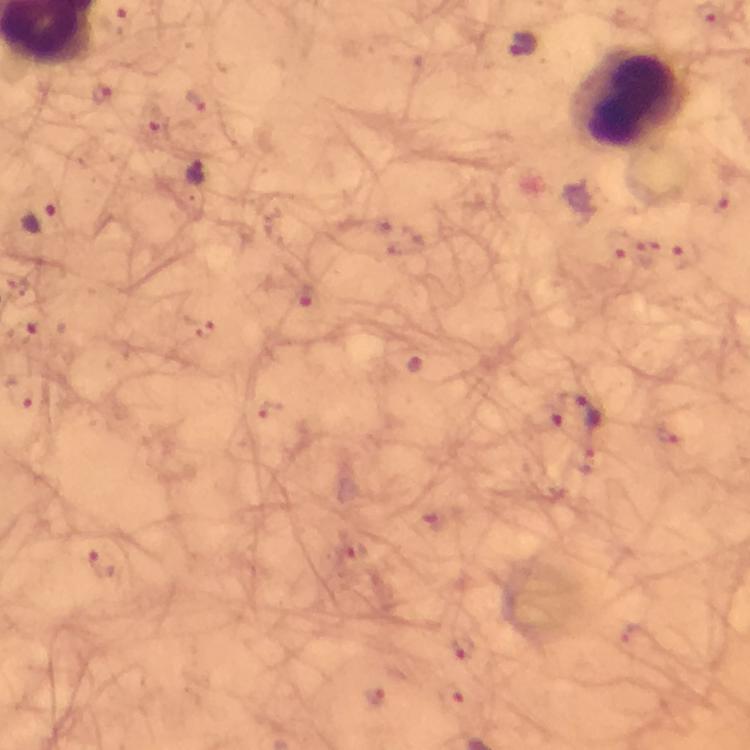 Approximate centers as {x, y} in pixels. Leukocyte locations: {630, 98}. Plasmodium parasite locations: {522, 47}, {195, 174}, {723, 204}, {38, 217}, {622, 243}, {685, 256}, {581, 409}, {103, 563}, {463, 648}. Image is 750×750 pixels. Immersion oil was used. Giemsa stain. 100x magnification. Thick smear. From a malaria diagnostic workup. Cropped region of a single field of view. Photographed through the microscope with a smartphone camera.